Locate every uninfected red blood cell.
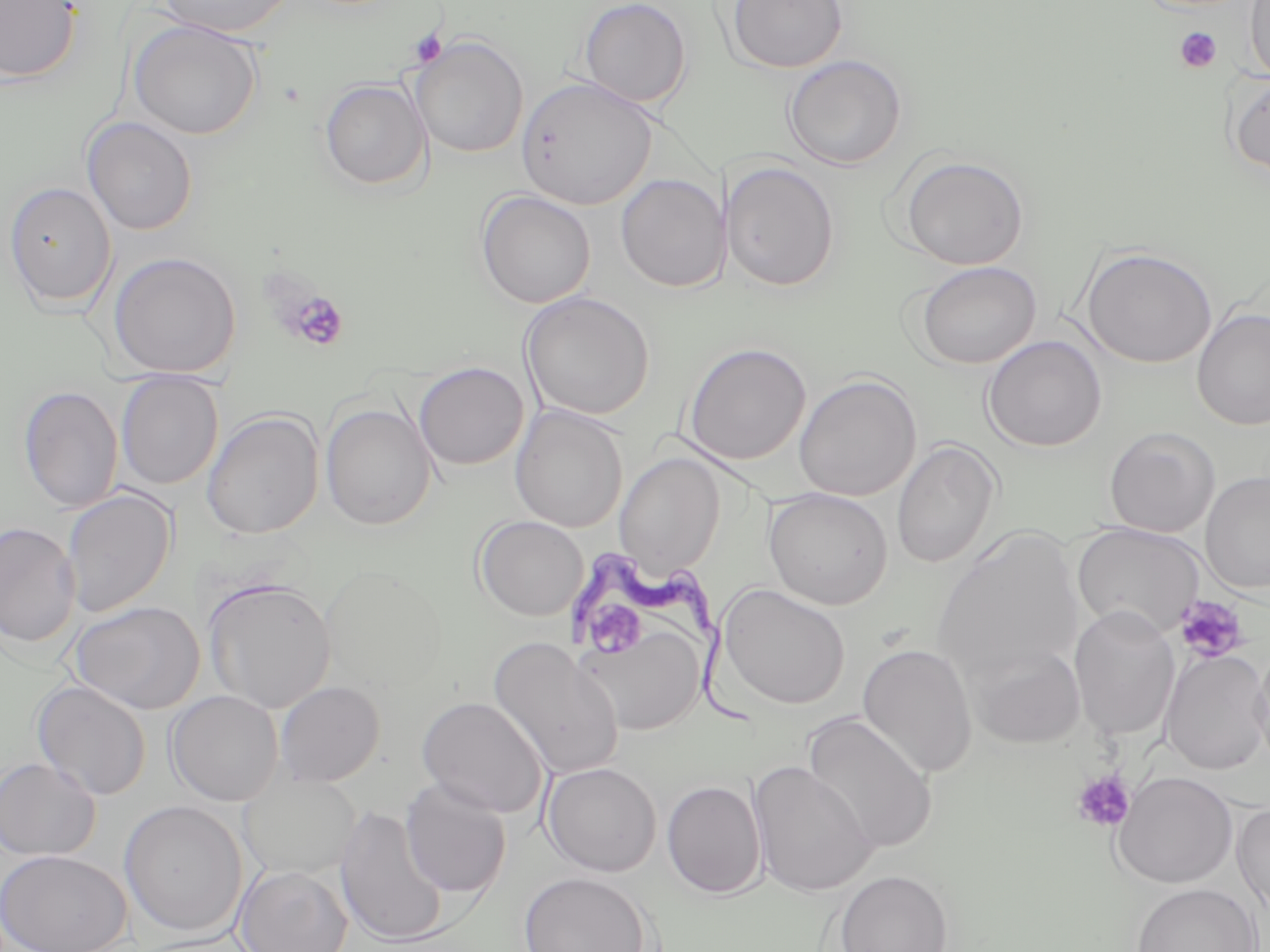
Approximate bounding boxes as named x1/y1/x2/y2 corners in pixels.
Uninfected red blood cells (subset): (x1=0, y1=0, x2=82, y2=84), (x1=155, y1=0, x2=297, y2=38), (x1=578, y1=0, x2=692, y2=109), (x1=726, y1=0, x2=848, y2=73), (x1=1244, y1=0, x2=1270, y2=85), (x1=128, y1=19, x2=262, y2=140), (x1=411, y1=36, x2=529, y2=158), (x1=782, y1=54, x2=907, y2=170), (x1=1227, y1=73, x2=1270, y2=179), (x1=516, y1=76, x2=657, y2=210), (x1=320, y1=79, x2=430, y2=191), (x1=81, y1=116, x2=198, y2=235), (x1=897, y1=155, x2=1029, y2=270), (x1=722, y1=160, x2=840, y2=292), (x1=616, y1=174, x2=728, y2=293), (x1=3, y1=181, x2=117, y2=311), (x1=476, y1=190, x2=596, y2=308), (x1=1081, y1=246, x2=1217, y2=368), (x1=108, y1=251, x2=241, y2=378), (x1=914, y1=260, x2=1042, y2=368), (x1=521, y1=291, x2=655, y2=420), (x1=1192, y1=308, x2=1270, y2=430), (x1=982, y1=335, x2=1106, y2=452), (x1=681, y1=342, x2=812, y2=466), (x1=413, y1=362, x2=529, y2=470), (x1=116, y1=372, x2=223, y2=490), (x1=793, y1=374, x2=921, y2=501), (x1=18, y1=384, x2=123, y2=513), (x1=320, y1=402, x2=438, y2=530), (x1=510, y1=406, x2=629, y2=533), (x1=202, y1=411, x2=324, y2=538), (x1=1103, y1=426, x2=1220, y2=537), (x1=892, y1=440, x2=1001, y2=568), (x1=614, y1=453, x2=725, y2=576), (x1=1200, y1=471, x2=1270, y2=595), (x1=61, y1=488, x2=176, y2=618), (x1=763, y1=488, x2=893, y2=610), (x1=474, y1=515, x2=588, y2=621), (x1=0, y1=521, x2=81, y2=648), (x1=933, y1=528, x2=1084, y2=683), (x1=319, y1=563, x2=448, y2=693), (x1=203, y1=578, x2=336, y2=714), (x1=716, y1=584, x2=851, y2=710), (x1=69, y1=601, x2=206, y2=715), (x1=1068, y1=605, x2=1181, y2=740), (x1=575, y1=618, x2=708, y2=738), (x1=488, y1=636, x2=624, y2=781), (x1=1251, y1=640, x2=1270, y2=775), (x1=966, y1=642, x2=1086, y2=749), (x1=857, y1=643, x2=978, y2=779), (x1=1160, y1=648, x2=1270, y2=775), (x1=32, y1=680, x2=152, y2=801), (x1=274, y1=680, x2=385, y2=786), (x1=166, y1=690, x2=284, y2=806), (x1=417, y1=696, x2=549, y2=819), (x1=802, y1=712, x2=938, y2=854), (x1=0, y1=757, x2=100, y2=861), (x1=749, y1=761, x2=878, y2=898), (x1=542, y1=762, x2=662, y2=877), (x1=1112, y1=771, x2=1238, y2=889), (x1=239, y1=774, x2=361, y2=879), (x1=400, y1=779, x2=511, y2=898), (x1=661, y1=780, x2=766, y2=899), (x1=119, y1=800, x2=248, y2=937), (x1=1232, y1=801, x2=1270, y2=924), (x1=334, y1=805, x2=449, y2=946), (x1=0, y1=849, x2=132, y2=952), (x1=234, y1=865, x2=353, y2=952), (x1=834, y1=869, x2=954, y2=952), (x1=518, y1=871, x2=652, y2=952), (x1=1131, y1=883, x2=1262, y2=952).

Summary:
  - Trypanosoma brucei locations: (x1=558, y1=545, x2=766, y2=728)
  - Platelet locations (subset): (x1=1174, y1=27, x2=1222, y2=73), (x1=408, y1=28, x2=448, y2=68), (x1=282, y1=289, x2=351, y2=353), (x1=1173, y1=595, x2=1250, y2=664), (x1=587, y1=597, x2=648, y2=656), (x1=1071, y1=770, x2=1136, y2=833)
  - Slide-level diagnosis: Trypanosoma brucei
  - Field of view: one of a larger specimen
  - Preparation: thin blood film
  - Image size: 1270×952 pixels
  - Magnification: 1000x
  - Modality: optical microscopy
  - Stain: May-Grünwald-Giemsa